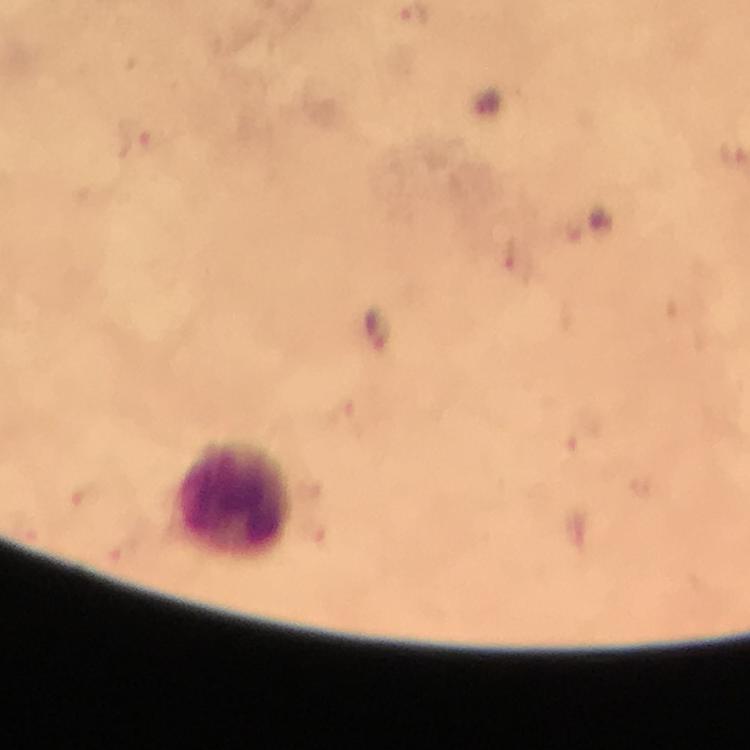

context: from a malaria diagnostic workup
leukocyte_locations: 'approximate object centers, in pixels from the top-left corner: (x=235, y=501)'
magnification: 100x
image_size: 750×750 pixels
stain: Giemsa
capture: smartphone camera through the microscope
immersion_oil: applied
malaria_parasite_locations: 'approximate object centers, in pixels from the top-left corner: (x=135, y=134), (x=379, y=333), (x=344, y=418)'
preparation: thick blood smear
cropped_from: one field of view